Outline each Trypanosoma brucei.
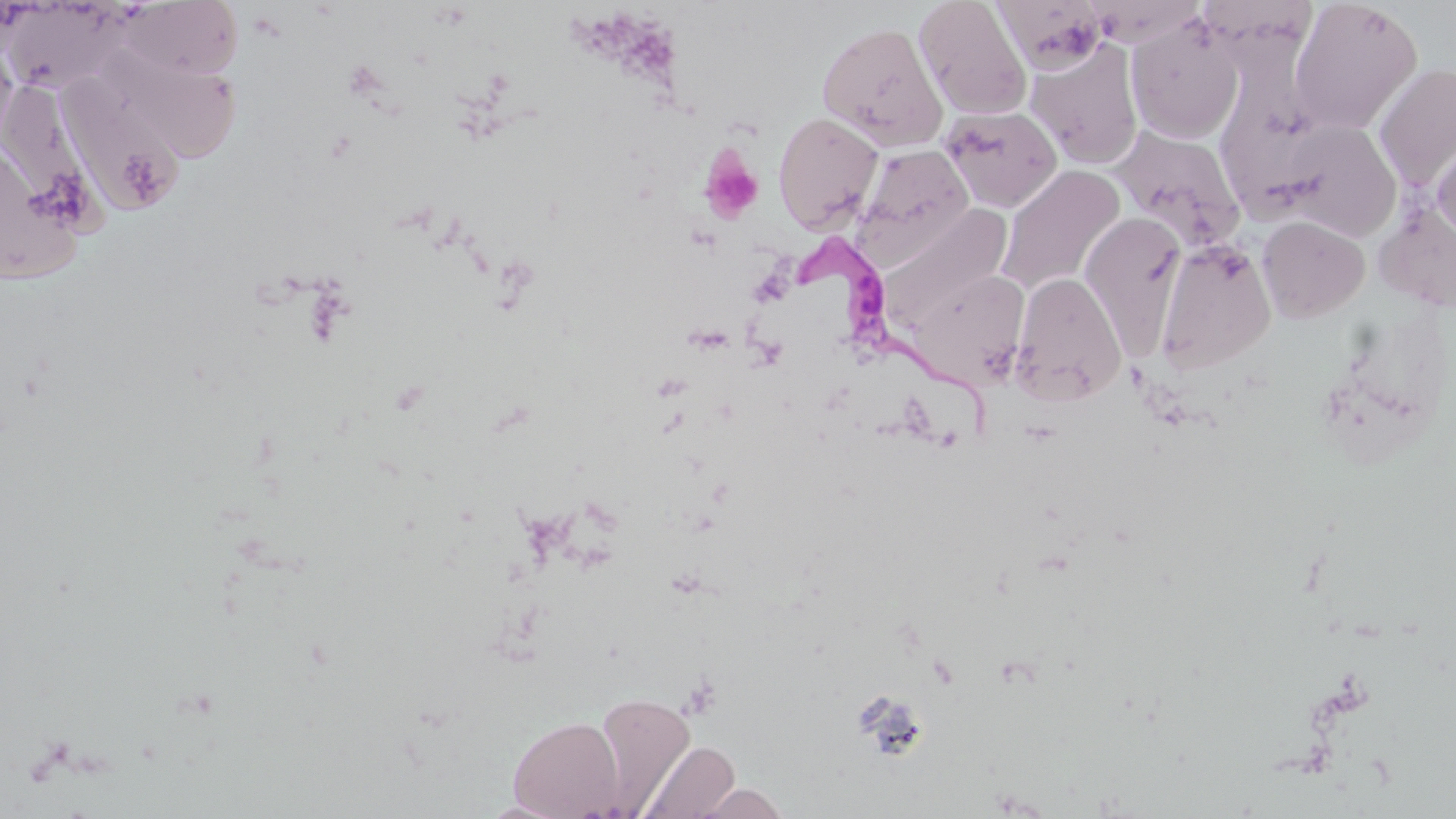
Approximate bounding boxes as (x1,y1)-(x2,y2) corner pairs in pixels.
Trypanosoma brucei: (791,236)-(991,435).

Uninfected red blood cell locations: (914,0)-(1032,120), (993,0)-(1110,74), (1288,0)-(1423,135), (116,1)-(244,80), (3,2)-(130,97), (1126,16)-(1245,144), (816,21)-(948,151), (0,40)-(19,149), (1025,40)-(1143,169), (98,51)-(241,163), (1373,62)-(1456,192), (60,84)-(189,212), (5,88)-(118,247), (1220,102)-(1344,224), (938,105)-(1063,212), (772,110)-(885,233), (1272,120)-(1402,240), (1108,125)-(1246,251), (1430,136)-(1456,245), (0,141)-(86,286), (853,144)-(975,266), (996,165)-(1126,296), (1375,202)-(1455,312), (886,206)-(1012,329), (1078,210)-(1187,354), (1257,215)-(1370,323), (1156,239)-(1275,374), (910,268)-(1031,388), (1011,273)-(1127,405), (593,692)-(696,813), (507,715)-(624,818), (637,740)-(740,819), (692,782)-(791,819). Platelet locations: (699,147)-(764,225). Slide-level diagnosis: Trypanosoma brucei. May-Grünwald-Giemsa stain. One field of a larger specimen. Image is 1456×819 pixels. Captured at 1000x magnification. Light microscopy. Thin blood film.